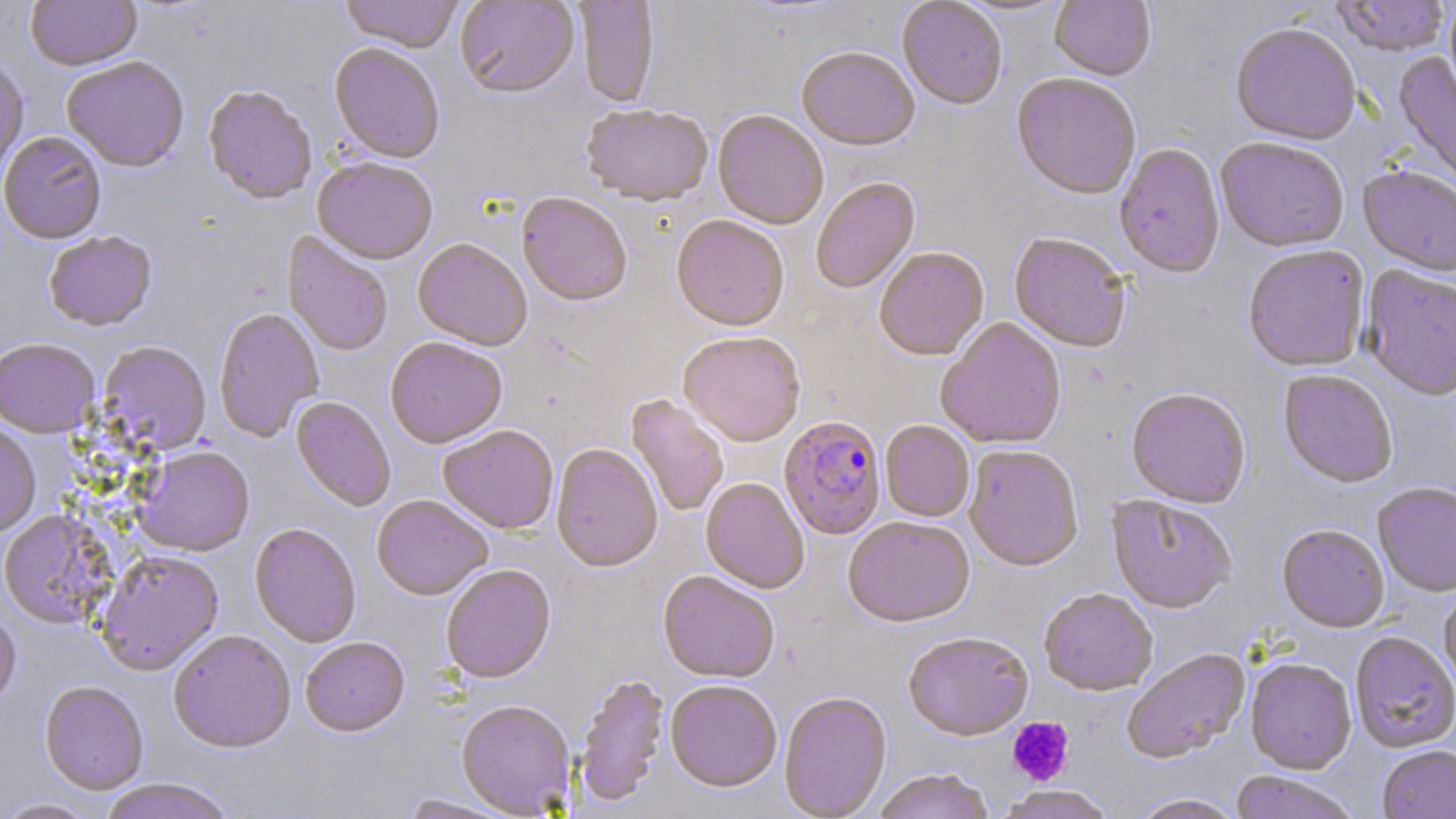

Approximate bounding boxes as (x1,y1)-(x2,y2) corner pairs in pixels. Platelet locations: (1007,717)-(1074,786). Plasmodium falciparum-infected red blood cell locations: (779,416)-(887,541). Uninfected red blood cell locations: (26,0)-(142,73), (338,0)-(464,55), (455,0)-(579,101), (574,0)-(660,109), (954,0)-(1071,17), (1050,0)-(1155,82), (1333,0)-(1450,57), (897,1)-(1008,112), (1444,1)-(1456,102), (1230,24)-(1361,147), (329,45)-(444,166), (797,49)-(919,153), (1393,51)-(1456,196), (62,58)-(189,174), (0,60)-(29,181), (1011,75)-(1141,202), (203,87)-(317,206), (581,106)-(713,209), (712,111)-(828,231), (0,132)-(107,245), (1215,138)-(1349,253), (1114,144)-(1225,279), (312,160)-(437,267), (1358,166)-(1456,277), (811,179)-(921,296), (517,195)-(631,309), (671,217)-(788,334), (282,232)-(393,357), (44,233)-(157,333), (1009,234)-(1131,354), (412,241)-(531,352), (1243,246)-(1369,372), (874,248)-(989,363), (1361,267)-(1456,401), (214,309)-(325,443), (936,318)-(1067,451), (678,334)-(806,449), (0,339)-(100,438), (385,339)-(507,451), (98,343)-(211,455), (1278,370)-(1398,489), (1126,389)-(1250,509), (625,395)-(730,517), (291,397)-(395,513), (880,421)-(974,523), (0,423)-(41,539), (438,427)-(558,535), (551,444)-(663,575), (965,446)-(1083,573), (134,447)-(255,559), (700,478)-(809,595), (1373,483)-(1456,598), (372,496)-(492,602), (1107,497)-(1236,615), (0,510)-(115,630), (843,518)-(974,630), (249,525)-(361,649), (1278,525)-(1389,633), (95,552)-(224,677), (441,566)-(555,685), (658,573)-(779,684), (1439,587)-(1456,694), (1039,590)-(1157,697), (0,611)-(20,713), (168,632)-(296,754), (903,633)-(1033,742), (1350,633)-(1456,753), (301,638)-(410,739), (1122,650)-(1251,764), (1245,659)-(1357,775), (575,673)-(670,810), (39,682)-(149,796), (665,682)-(782,795), (779,693)-(892,818), (457,702)-(576,817), (1377,747)-(1456,819), (872,770)-(995,819), (1229,772)-(1359,819), (98,780)-(237,819), (999,786)-(1115,819), (400,795)-(517,819), (1130,795)-(1245,819), (0,799)-(102,819). Slide-level diagnosis: Plasmodium falciparum. Light microscopy. Captured at 1000x magnification. May-Grünwald-Giemsa-stained preparation. Single field of view. Thin blood film. Image is 1456×819 pixels.